Name the parasite shown.
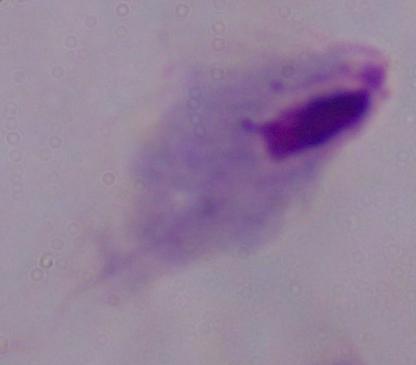

A trichomonad.

Captured at 1000x magnification. Photomicrograph.